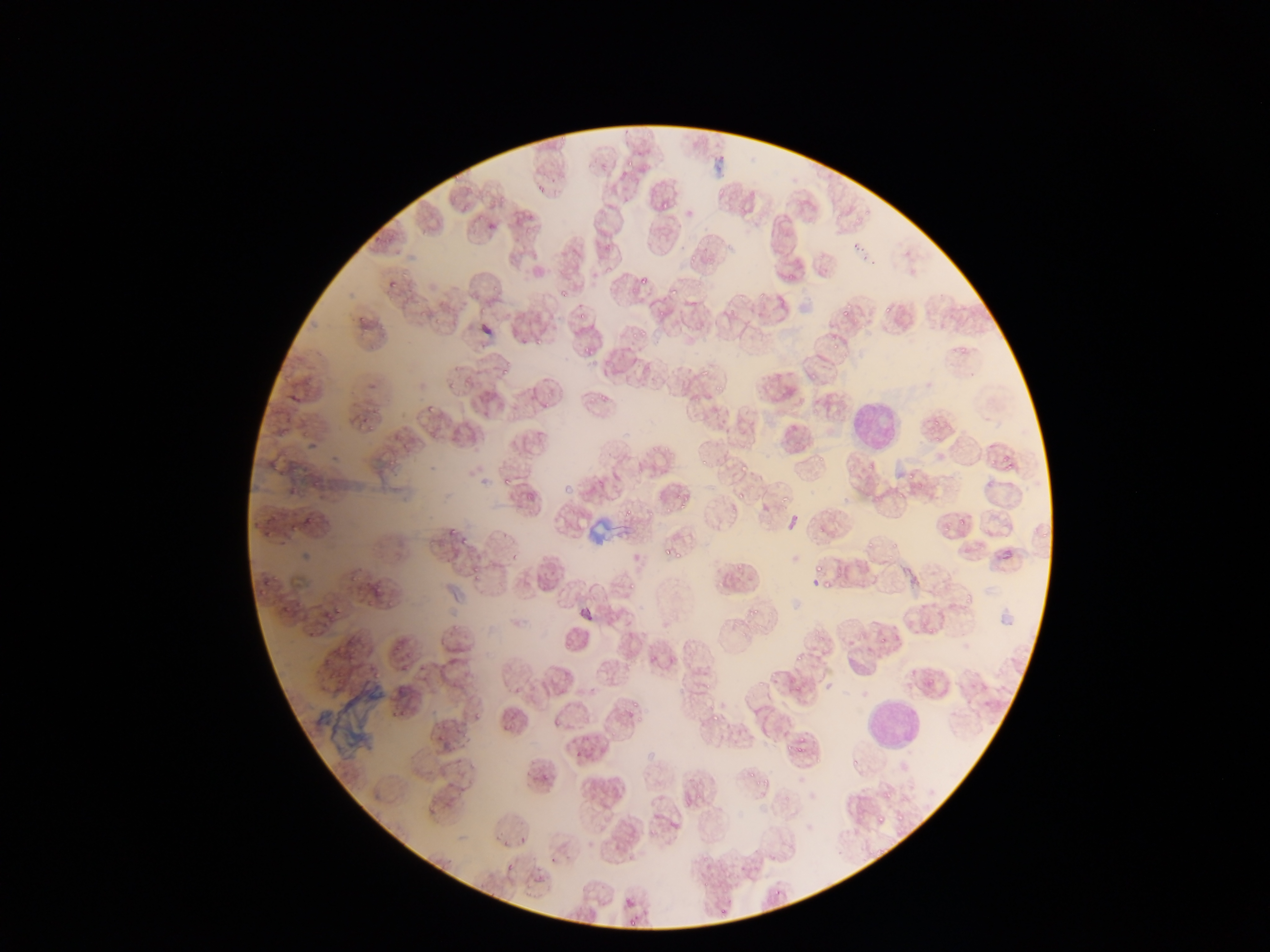

Approximate bounding boxes as left top right bottom in pixels. Leukocyte locations: 844 392 906 455; 863 695 922 755. Plasmodium parasite locations: 626 161 634 166; 452 172 459 183; 536 181 547 192; 653 192 676 216; 452 194 463 203; 498 194 506 202; 462 204 470 210; 687 250 696 264; 400 272 408 277; 637 273 654 289; 786 275 795 282; 388 282 397 290; 493 286 499 294; 559 287 570 302; 665 287 677 299; 758 292 766 300; 478 303 489 311; 841 306 852 317; 884 306 892 314; 727 308 734 316; 579 311 589 320; 656 312 664 319; 434 317 442 325; 639 324 649 336; 831 338 843 349; 535 339 541 347; 584 340 601 357; 454 363 462 371; 502 368 509 376; 701 370 709 376; 809 371 817 379; 446 383 455 391; 714 383 727 394; 595 391 610 401; 360 421 370 426; 1002 450 1013 463; 816 451 825 462; 701 456 707 464; 1006 462 1014 474; 906 469 914 481; 782 489 791 503; 897 493 907 501; 680 494 688 510; 734 494 750 502; 647 508 655 515; 664 508 675 517; 624 509 634 517; 958 520 966 529; 291 524 299 531; 263 526 269 536; 448 528 456 538; 1042 533 1047 541; 460 539 468 547; 866 539 874 545; 891 540 897 548; 661 547 670 554; 672 547 684 565; 510 553 518 561; 737 564 745 571; 809 565 826 574; 471 566 480 572; 264 577 270 586; 716 581 725 590; 258 584 264 596; 822 584 832 591; 374 586 382 593; 966 596 974 603; 749 598 766 618; 387 599 396 607; 283 601 292 611; 334 606 342 613; 328 614 334 623; 927 627 935 630; 308 629 315 638; 795 654 802 662; 402 664 408 672; 929 678 938 684; 704 681 711 689; 633 701 638 709; 709 708 729 723; 475 711 482 719; 639 717 647 724; 505 721 511 730; 796 743 804 752; 749 769 756 777; 763 775 769 786; 886 808 908 833; 874 813 891 830; 719 909 727 915; 629 919 635 928 | approximate x y pixel centers of objects too small to bound: 866 214; 481 217; 858 220; 873 265; 361 318; 635 335; 964 350; 952 351; 429 411; 936 423; 371 430; 282 435; 937 438; 991 461; 506 481; 946 529; 352 579; 476 579; 632 586; 881 642; 653 656; 774 675; 761 684; 555 722; 756 784; 696 794. Collected in Ghana. Image is 1270×952 pixels. Thin blood film. Single field of view. Photographed through a microscope with a mobile-phone camera.